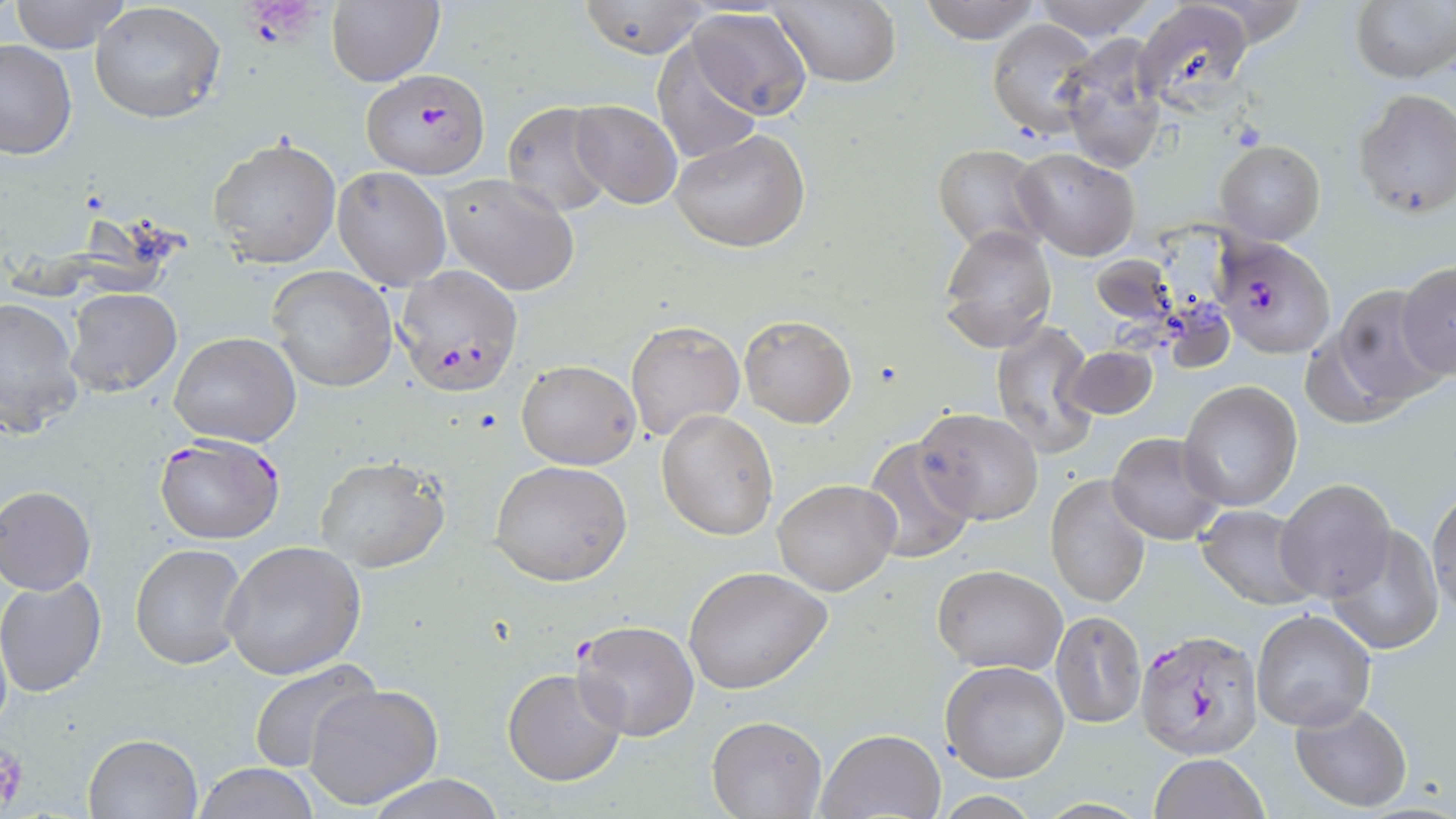
slide-level diagnosis = Plasmodium falciparum
magnification = 1000x
preparation = thin blood film
uninfected red blood cell locations = approximate bounding boxes as named x1/y1/x2/y2 corners in pixels: (x1=8, y1=0, x2=134, y2=53), (x1=767, y1=0, x2=900, y2=89), (x1=918, y1=0, x2=1040, y2=44), (x1=1030, y1=0, x2=1159, y2=41), (x1=1133, y1=0, x2=1253, y2=107), (x1=1349, y1=0, x2=1456, y2=85), (x1=327, y1=1, x2=444, y2=86), (x1=573, y1=1, x2=713, y2=58), (x1=90, y1=2, x2=226, y2=123), (x1=686, y1=6, x2=815, y2=120), (x1=986, y1=19, x2=1099, y2=139), (x1=1057, y1=38, x2=1168, y2=174), (x1=650, y1=39, x2=764, y2=167), (x1=0, y1=40, x2=76, y2=160), (x1=1352, y1=89, x2=1456, y2=219), (x1=569, y1=100, x2=683, y2=208), (x1=503, y1=102, x2=614, y2=217), (x1=671, y1=129, x2=811, y2=252), (x1=209, y1=136, x2=342, y2=269), (x1=1215, y1=140, x2=1326, y2=244), (x1=933, y1=145, x2=1049, y2=255), (x1=1015, y1=147, x2=1139, y2=259), (x1=332, y1=166, x2=451, y2=291), (x1=440, y1=174, x2=582, y2=296), (x1=939, y1=224, x2=1057, y2=352), (x1=1092, y1=255, x2=1175, y2=328), (x1=1394, y1=263, x2=1456, y2=380), (x1=265, y1=266, x2=398, y2=392), (x1=1320, y1=286, x2=1446, y2=415), (x1=64, y1=287, x2=182, y2=396), (x1=0, y1=295, x2=84, y2=439), (x1=737, y1=315, x2=856, y2=427), (x1=626, y1=319, x2=746, y2=442), (x1=991, y1=319, x2=1097, y2=458), (x1=170, y1=330, x2=301, y2=447), (x1=1062, y1=346, x2=1158, y2=421), (x1=516, y1=358, x2=641, y2=470), (x1=1178, y1=380, x2=1302, y2=512), (x1=914, y1=409, x2=1043, y2=527), (x1=657, y1=410, x2=779, y2=540), (x1=1108, y1=431, x2=1226, y2=544), (x1=861, y1=438, x2=977, y2=563), (x1=314, y1=455, x2=449, y2=573), (x1=489, y1=459, x2=632, y2=586), (x1=1045, y1=475, x2=1151, y2=609), (x1=1275, y1=478, x2=1397, y2=602), (x1=773, y1=479, x2=900, y2=596), (x1=0, y1=485, x2=95, y2=595), (x1=1429, y1=487, x2=1456, y2=621), (x1=1195, y1=503, x2=1317, y2=608), (x1=1328, y1=525, x2=1444, y2=658), (x1=219, y1=540, x2=367, y2=680), (x1=129, y1=542, x2=249, y2=669), (x1=933, y1=565, x2=1067, y2=674), (x1=682, y1=566, x2=831, y2=696), (x1=0, y1=576, x2=107, y2=696), (x1=1251, y1=608, x2=1378, y2=734), (x1=1051, y1=610, x2=1146, y2=729), (x1=574, y1=619, x2=700, y2=742), (x1=246, y1=660, x2=381, y2=777), (x1=940, y1=661, x2=1070, y2=783), (x1=503, y1=668, x2=627, y2=786), (x1=303, y1=682, x2=443, y2=810), (x1=1290, y1=701, x2=1412, y2=813), (x1=706, y1=716, x2=828, y2=818), (x1=815, y1=727, x2=946, y2=817), (x1=83, y1=733, x2=202, y2=819), (x1=1147, y1=753, x2=1270, y2=819), (x1=193, y1=763, x2=321, y2=819), (x1=359, y1=774, x2=513, y2=819)
modality = optical microscopy
Plasmodium falciparum-infected red blood cell locations = approximate bounding boxes as named x1/y1/x2/y2 corners in pixels: (x1=362, y1=70, x2=491, y2=181), (x1=1208, y1=239, x2=1335, y2=361), (x1=393, y1=266, x2=522, y2=394), (x1=154, y1=433, x2=287, y2=545), (x1=1134, y1=627, x2=1264, y2=759)
field of view = single
stain = May-Grünwald-Giemsa
platelet locations = approximate bounding boxes as named x1/y1/x2/y2 corners in pixels: (x1=248, y1=3, x2=320, y2=44), (x1=1, y1=742, x2=27, y2=811)
image size = 1456×819 pixels